Identify the parasite.
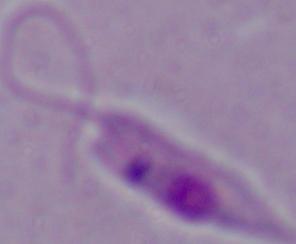

This is Leishmania.

modality = micrograph
magnification = 1000x